Locate every Plasmodium parasite.
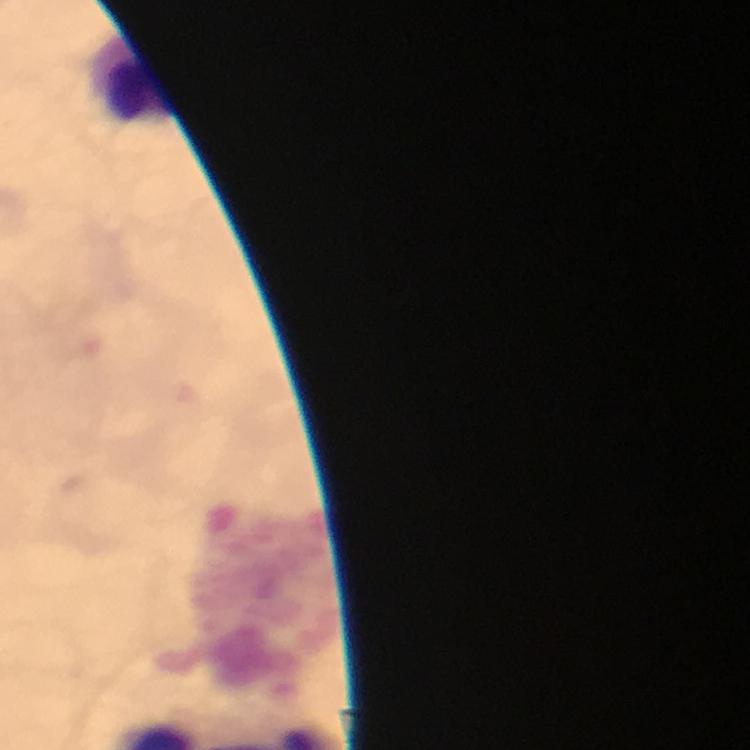

No Plasmodium parasites seen.

Approximate object centers, in pixels from the top-left corner.
Summary:
  - Leukocyte locations: (x=136, y=79)
  - Immersion oil: applied
  - Stain: Giemsa
  - Capture: smartphone photograph through a microscope
  - Cropped from: a single field of view
  - Image size: 750×750 pixels
  - Magnification: 100x
  - Preparation: thick blood smear
  - Context: from a malaria diagnostic workup